Describe the morphology of the erythrocytes.
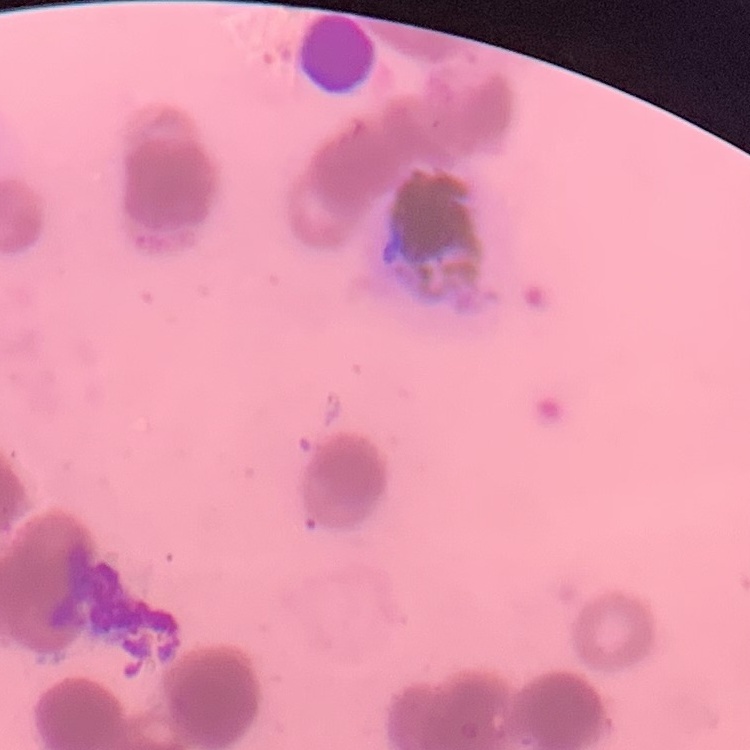

Rouleaux formation.

Square crop of a larger photomicrograph. Thin peripheral smear. Stained with either Field's or Giemsa.